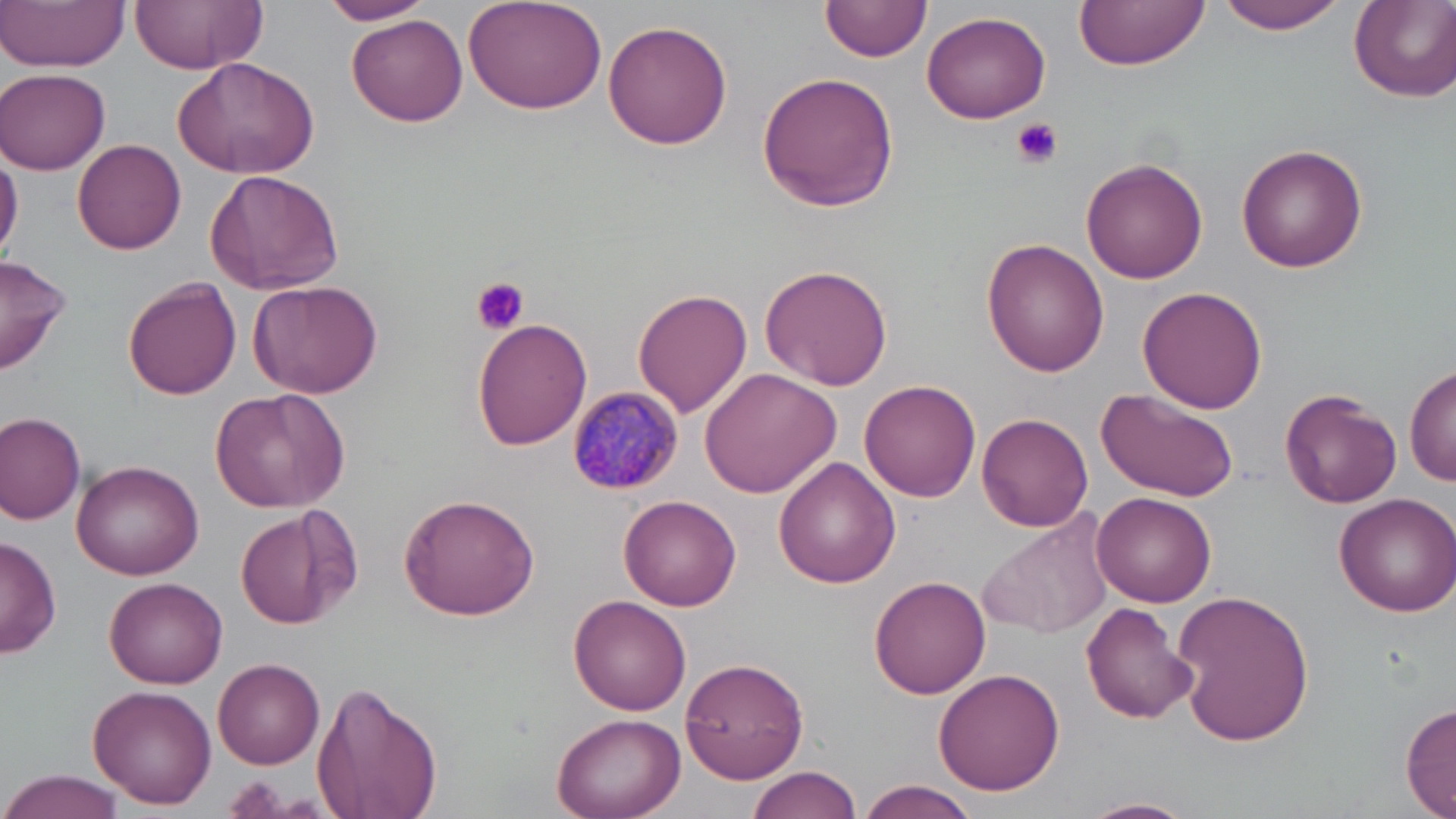

Summary:
  - Coordinate format: approximate bounding boxes as (x1, y1, x2, y2) in pixels
  - Uninfected red blood cell locations: (2, 0, 129, 72), (131, 0, 263, 73), (319, 0, 434, 26), (463, 0, 606, 114), (822, 0, 934, 63), (1074, 0, 1206, 74), (1215, 0, 1354, 36), (1348, 2, 1456, 104), (922, 11, 1052, 124), (347, 13, 467, 126), (603, 21, 733, 150), (171, 56, 321, 181), (2, 67, 110, 174), (756, 72, 901, 212), (73, 139, 188, 254), (1236, 141, 1369, 272), (0, 149, 23, 263), (1080, 157, 1206, 285), (206, 169, 345, 295), (982, 239, 1110, 376), (0, 253, 72, 375), (760, 263, 894, 390), (124, 277, 240, 399), (248, 278, 385, 398), (1136, 286, 1268, 413), (634, 287, 753, 416), (472, 317, 594, 450), (1406, 363, 1456, 486), (702, 367, 843, 499), (860, 378, 981, 501), (211, 385, 350, 513), (1280, 387, 1402, 509), (1097, 389, 1244, 505), (0, 412, 86, 527), (976, 412, 1092, 533), (772, 456, 900, 588), (70, 460, 204, 581), (1091, 491, 1217, 606), (618, 492, 741, 610), (1333, 492, 1456, 617), (398, 493, 541, 621), (234, 507, 354, 629), (979, 510, 1114, 641), (0, 534, 60, 660), (105, 575, 228, 688), (871, 575, 992, 699), (1171, 589, 1315, 748), (568, 594, 692, 715), (1080, 601, 1199, 726), (213, 658, 325, 769), (681, 658, 809, 783), (932, 667, 1062, 796), (311, 680, 444, 819), (88, 683, 217, 809), (1400, 703, 1456, 818), (549, 712, 685, 819), (746, 766, 866, 819), (0, 769, 124, 817), (855, 780, 980, 819), (1079, 797, 1196, 819)
  - Plasmodium malariae-infected red blood cell locations: (565, 386, 683, 497)
  - Platelet locations: (1012, 118, 1064, 168), (471, 278, 528, 336)
  - Slide-level diagnosis: Plasmodium malariae
  - Preparation: thin blood film
  - Modality: optical microscopy
  - Image size: 1456×819 pixels
  - Magnification: 1000x
  - Stain: May-Grünwald-Giemsa
  - Field of view: single